Locate every Plasmodium parasite.
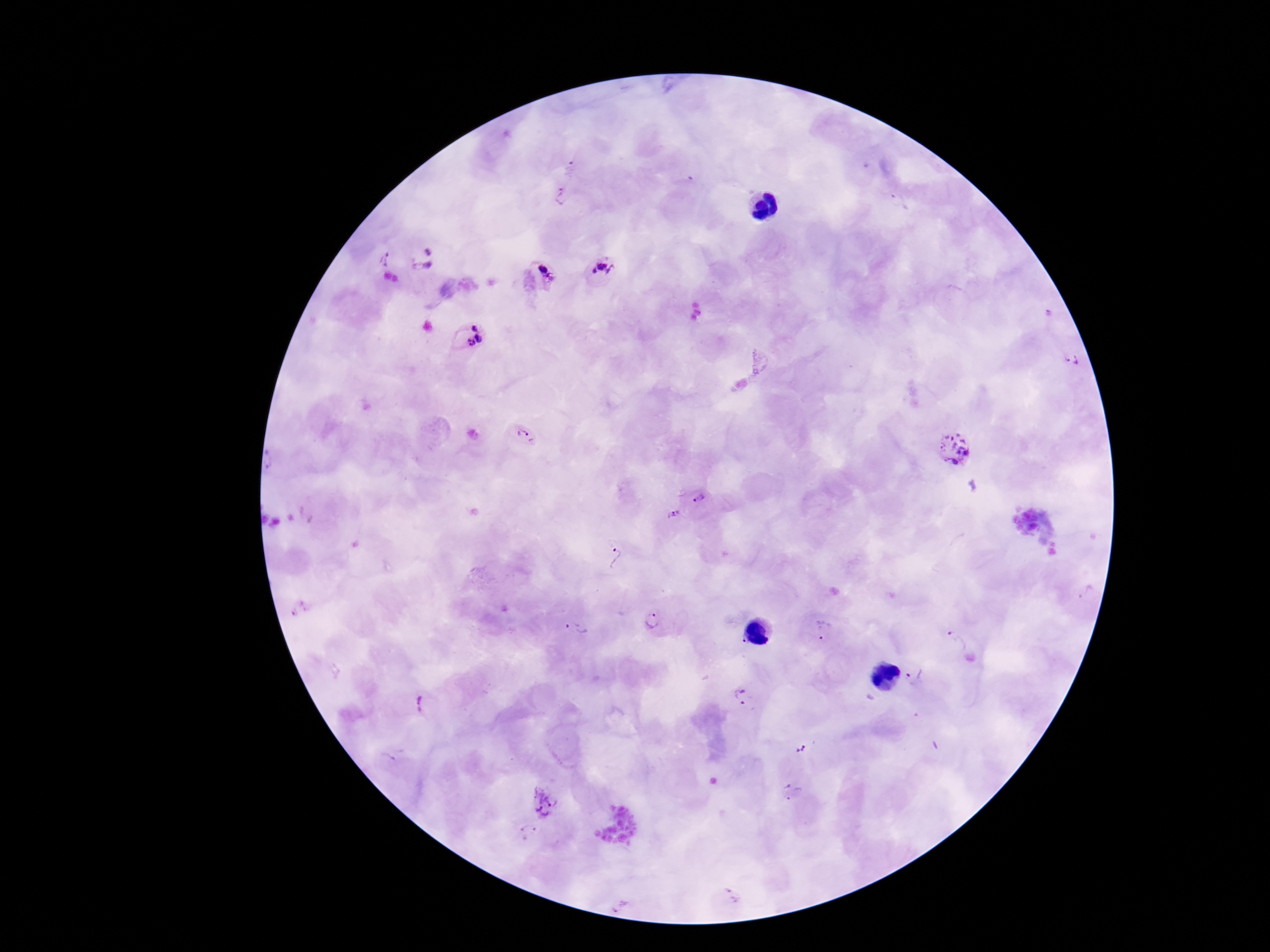

Approximate centers as [x, y] in pixels.
Plasmodium parasites: [571, 168], [561, 197], [428, 250], [389, 259], [424, 267], [603, 270], [544, 275], [476, 326], [482, 338], [471, 343], [1071, 359], [524, 436], [955, 450], [699, 498], [673, 511], [615, 557], [1087, 593], [302, 609], [654, 623], [575, 630], [823, 632], [740, 641], [957, 642], [916, 678], [742, 697], [424, 702], [800, 751], [791, 791], [545, 799], [527, 832], [732, 896], [619, 904].

Patient malaria status: positive. Thick peripheral-blood smear. One field from this slide. Giemsa-stained preparation. 100x magnification. Smartphone photograph taken through the microscope eyepiece. Image is 1270×952 pixels.